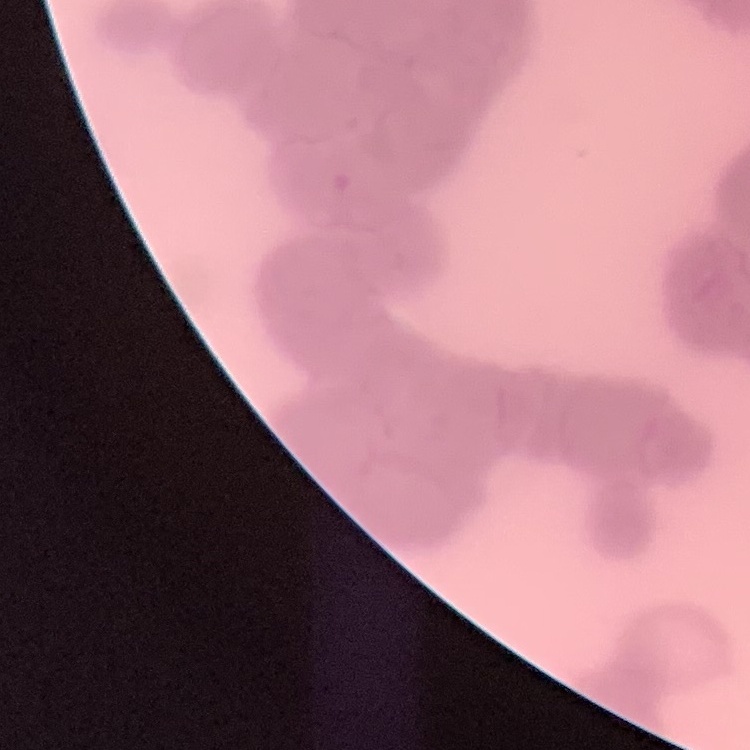

Summary:
  - Red blood cell morphology: rouleaux formation
  - Stain: Field's or Giemsa
  - Preparation: thin blood film
  - Image type: one tile cut from a larger photomicrograph